Give the extent of all Plasmodium vivax-infected red blood cells.
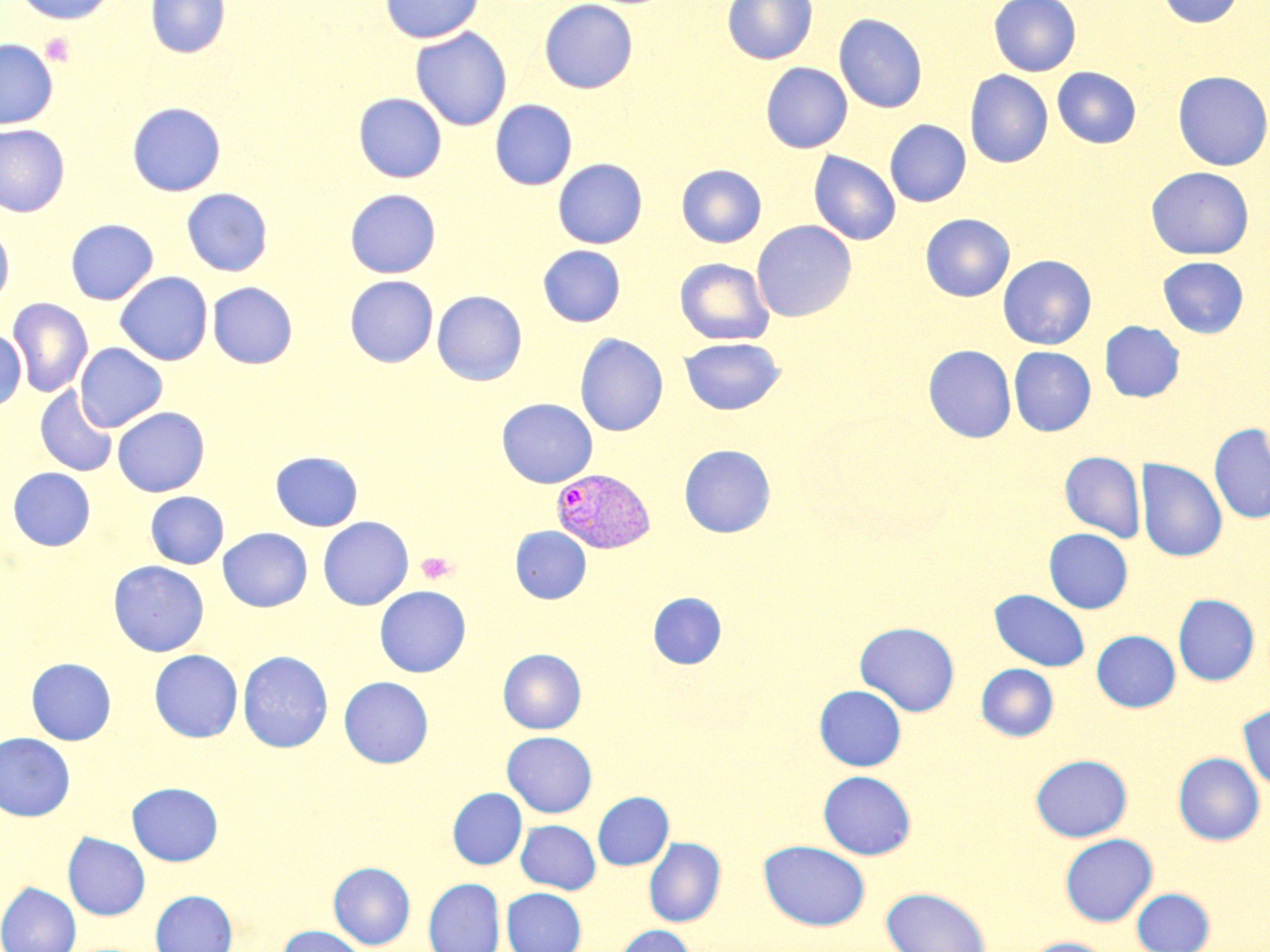

Approximate bounding boxes as (x1, y1, x2, y2) in pixels.
Plasmodium vivax-infected red blood cells: (551, 468, 655, 555).

Platelet locations: (40, 33, 75, 66), (416, 551, 457, 584). Uninfected red blood cell locations: (12, 0, 116, 25), (145, 0, 230, 58), (379, 0, 485, 43), (539, 0, 638, 93), (722, 0, 818, 65), (989, 0, 1081, 76), (1156, 0, 1243, 27), (834, 13, 927, 113), (410, 28, 512, 131), (0, 38, 58, 129), (760, 62, 853, 153), (1052, 67, 1141, 148), (964, 70, 1052, 169), (1172, 71, 1270, 171), (354, 93, 447, 183), (490, 100, 577, 190), (127, 102, 226, 196), (885, 119, 971, 207), (0, 124, 70, 217), (809, 151, 901, 246), (552, 158, 648, 248), (676, 164, 766, 248), (1146, 167, 1254, 259), (181, 188, 273, 276), (344, 188, 441, 278), (920, 214, 1014, 301), (65, 219, 158, 304), (752, 220, 856, 322), (0, 225, 13, 307), (538, 245, 626, 327), (997, 255, 1097, 350), (1158, 256, 1249, 338), (675, 258, 775, 345), (115, 272, 213, 366), (344, 275, 438, 367), (207, 282, 297, 368), (432, 290, 527, 385), (7, 298, 93, 397), (1099, 320, 1185, 402), (0, 329, 27, 411), (575, 333, 669, 436), (679, 337, 785, 415), (75, 343, 167, 432), (923, 344, 1017, 443), (1008, 347, 1096, 436), (35, 386, 118, 477), (496, 398, 598, 487), (112, 407, 210, 496), (1209, 423, 1270, 524), (679, 444, 776, 537), (270, 451, 363, 531), (1059, 451, 1145, 542), (1136, 458, 1227, 562), (8, 467, 96, 551), (145, 491, 228, 569), (318, 516, 414, 610), (510, 526, 591, 604), (218, 527, 312, 612), (1043, 528, 1133, 613), (108, 561, 209, 657), (374, 586, 471, 677), (990, 589, 1090, 671), (648, 592, 726, 669), (1172, 594, 1259, 685), (854, 621, 960, 717), (1092, 630, 1180, 712), (498, 648, 586, 733), (149, 649, 242, 742), (238, 650, 332, 753), (25, 657, 116, 745), (976, 663, 1059, 741), (338, 676, 433, 768), (814, 685, 906, 771), (1238, 702, 1270, 795), (502, 731, 597, 817), (0, 732, 75, 821), (1173, 752, 1265, 845), (1030, 754, 1132, 842), (818, 770, 916, 860), (127, 782, 222, 866), (448, 788, 527, 869), (593, 791, 673, 870), (516, 820, 600, 894), (62, 832, 150, 920), (1059, 833, 1157, 926), (644, 837, 725, 927), (759, 840, 870, 930), (328, 862, 415, 950), (423, 878, 505, 952), (0, 882, 81, 952), (502, 887, 586, 952), (881, 887, 991, 952), (1131, 887, 1215, 952), (151, 889, 237, 952), (277, 925, 368, 952), (613, 925, 696, 952), (1024, 937, 1114, 952). Slide-level diagnosis: Plasmodium vivax. May-Grünwald-Giemsa-stained preparation. Image is 1270×952 pixels. One field of a larger specimen. Thin blood film. 1000x magnification. Optical microscopy.